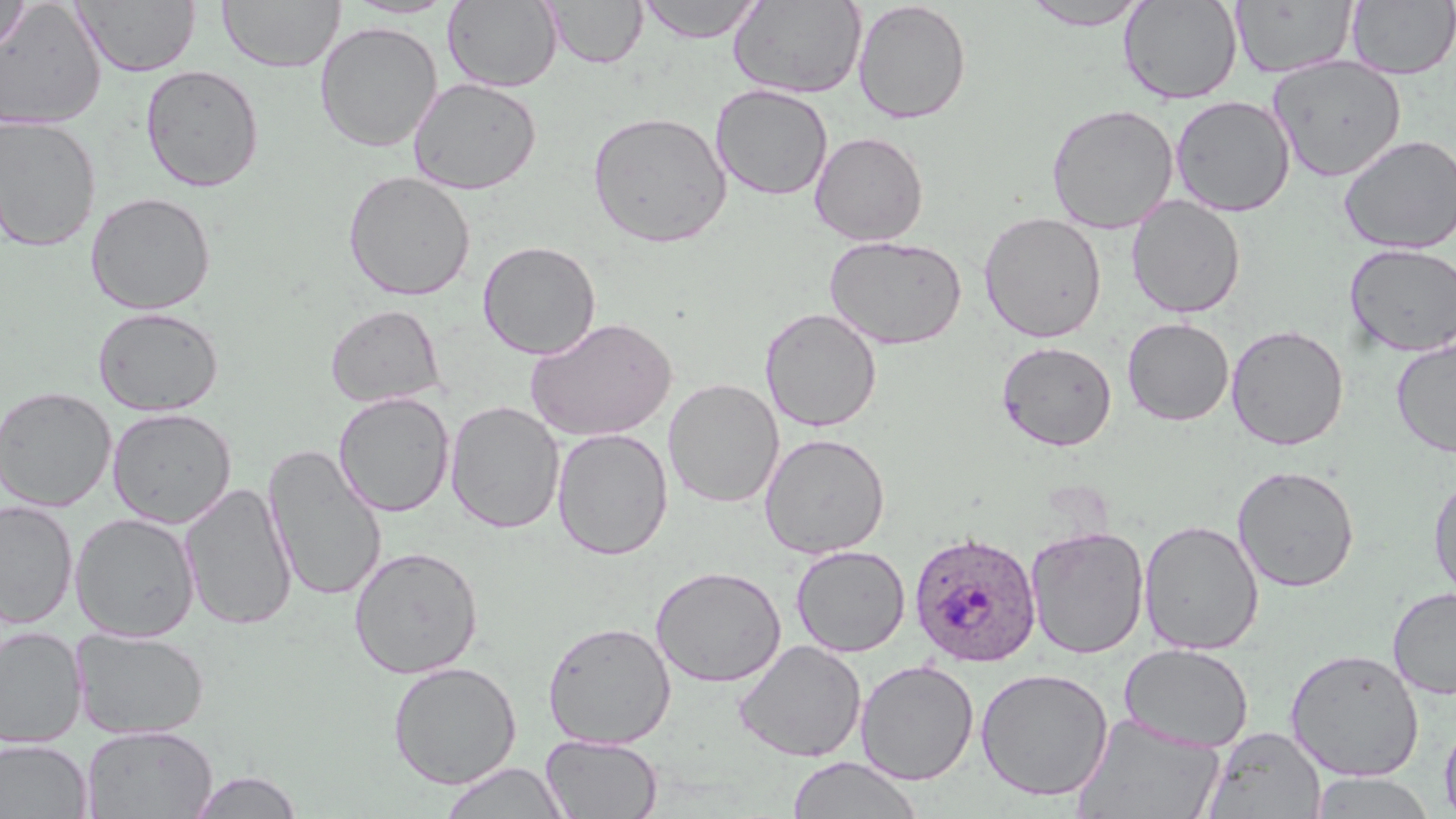 Approximate bounding boxes as named x1/y1/x2/y2 corners in pixels. Plasmodium ovale-infected red blood cell locations: (x1=908, y1=530, x2=1042, y2=667). Uninfected red blood cell locations: (x1=74, y1=0, x2=200, y2=77), (x1=217, y1=0, x2=345, y2=73), (x1=638, y1=0, x2=765, y2=43), (x1=1230, y1=0, x2=1357, y2=78), (x1=0, y1=1, x2=31, y2=58), (x1=343, y1=1, x2=460, y2=19), (x1=443, y1=1, x2=562, y2=92), (x1=545, y1=1, x2=647, y2=68), (x1=728, y1=1, x2=866, y2=99), (x1=852, y1=1, x2=972, y2=124), (x1=1021, y1=1, x2=1153, y2=30), (x1=1118, y1=1, x2=1243, y2=103), (x1=1347, y1=1, x2=1455, y2=79), (x1=0, y1=2, x2=107, y2=130), (x1=314, y1=21, x2=443, y2=152), (x1=1267, y1=57, x2=1407, y2=182), (x1=140, y1=64, x2=265, y2=192), (x1=408, y1=76, x2=542, y2=195), (x1=711, y1=84, x2=833, y2=201), (x1=1170, y1=95, x2=1295, y2=217), (x1=1046, y1=103, x2=1179, y2=234), (x1=586, y1=111, x2=733, y2=248), (x1=0, y1=115, x2=102, y2=252), (x1=809, y1=130, x2=929, y2=246), (x1=1339, y1=134, x2=1456, y2=255), (x1=342, y1=170, x2=476, y2=301), (x1=85, y1=191, x2=216, y2=315), (x1=1126, y1=195, x2=1247, y2=319), (x1=978, y1=211, x2=1107, y2=343), (x1=824, y1=235, x2=968, y2=350), (x1=478, y1=240, x2=601, y2=359), (x1=1344, y1=243, x2=1456, y2=357), (x1=326, y1=304, x2=446, y2=408), (x1=92, y1=306, x2=224, y2=416), (x1=759, y1=307, x2=882, y2=432), (x1=525, y1=316, x2=677, y2=442), (x1=1122, y1=317, x2=1234, y2=426), (x1=1226, y1=324, x2=1349, y2=450), (x1=1391, y1=338, x2=1456, y2=459), (x1=996, y1=340, x2=1118, y2=451), (x1=663, y1=378, x2=784, y2=508), (x1=0, y1=385, x2=117, y2=512), (x1=333, y1=391, x2=455, y2=517), (x1=445, y1=400, x2=565, y2=533), (x1=106, y1=407, x2=237, y2=528), (x1=552, y1=427, x2=673, y2=560), (x1=759, y1=432, x2=890, y2=559), (x1=263, y1=444, x2=388, y2=602), (x1=1232, y1=464, x2=1360, y2=592), (x1=1428, y1=473, x2=1456, y2=605), (x1=180, y1=481, x2=298, y2=631), (x1=0, y1=500, x2=78, y2=628), (x1=69, y1=512, x2=200, y2=642), (x1=1138, y1=519, x2=1265, y2=655), (x1=1026, y1=525, x2=1149, y2=659), (x1=791, y1=544, x2=910, y2=657), (x1=348, y1=545, x2=484, y2=679), (x1=651, y1=565, x2=786, y2=687), (x1=1387, y1=587, x2=1456, y2=700), (x1=542, y1=621, x2=677, y2=749), (x1=0, y1=627, x2=87, y2=748), (x1=70, y1=627, x2=211, y2=739), (x1=733, y1=639, x2=866, y2=763), (x1=1118, y1=642, x2=1254, y2=752), (x1=1285, y1=648, x2=1425, y2=782), (x1=855, y1=660, x2=979, y2=785), (x1=387, y1=661, x2=522, y2=789), (x1=975, y1=666, x2=1113, y2=802), (x1=1073, y1=713, x2=1225, y2=818), (x1=1439, y1=715, x2=1456, y2=819), (x1=81, y1=724, x2=218, y2=819), (x1=1202, y1=726, x2=1326, y2=818), (x1=540, y1=734, x2=663, y2=818), (x1=0, y1=739, x2=93, y2=819), (x1=787, y1=755, x2=924, y2=819), (x1=438, y1=761, x2=571, y2=818), (x1=188, y1=769, x2=304, y2=818), (x1=1308, y1=772, x2=1438, y2=818). Slide-level diagnosis: Plasmodium ovale. Optical microscopy. May-Grünwald-Giemsa-stained preparation. Captured at 1000x magnification. Image is 1456×819 pixels. One field of a larger specimen. Thin blood film.